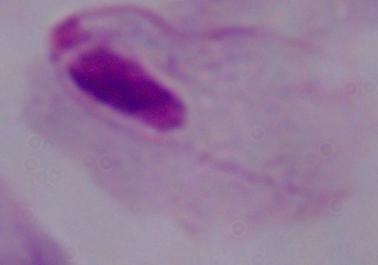

magnification = 1000x
modality = micrograph
identification = trichomonad